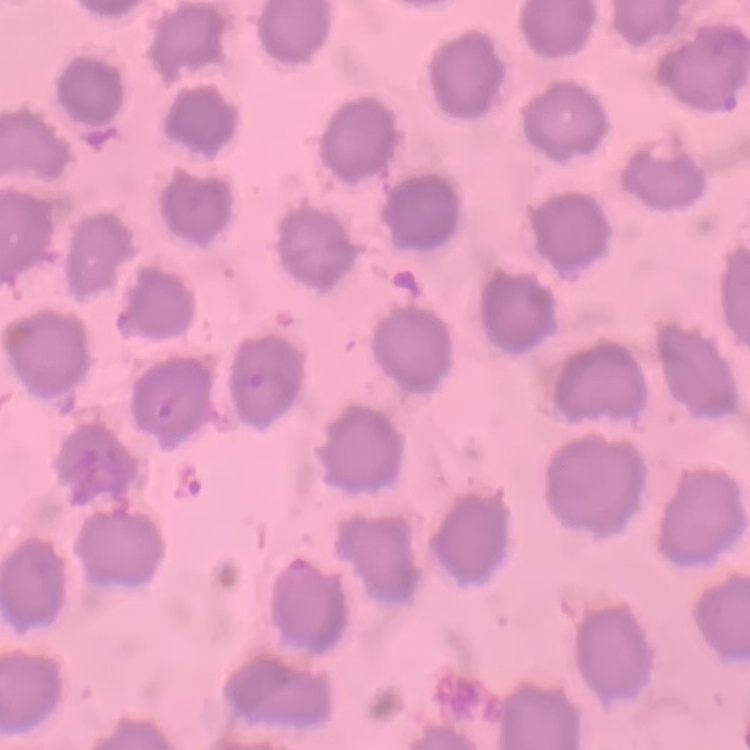
red_blood_cell_morphology: no rouleaux formation
preparation: thin blood smear
image_type: square crop of a larger photomicrograph
stain: Field's or Giemsa